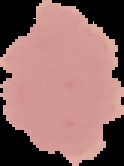
result = no Plasmodium parasites seen
image type = segmented cell region with the area outside set to black
image size = 124×166 pixels
preparation = thin blood smear